Give the position of every Plasmodium parasite visible.
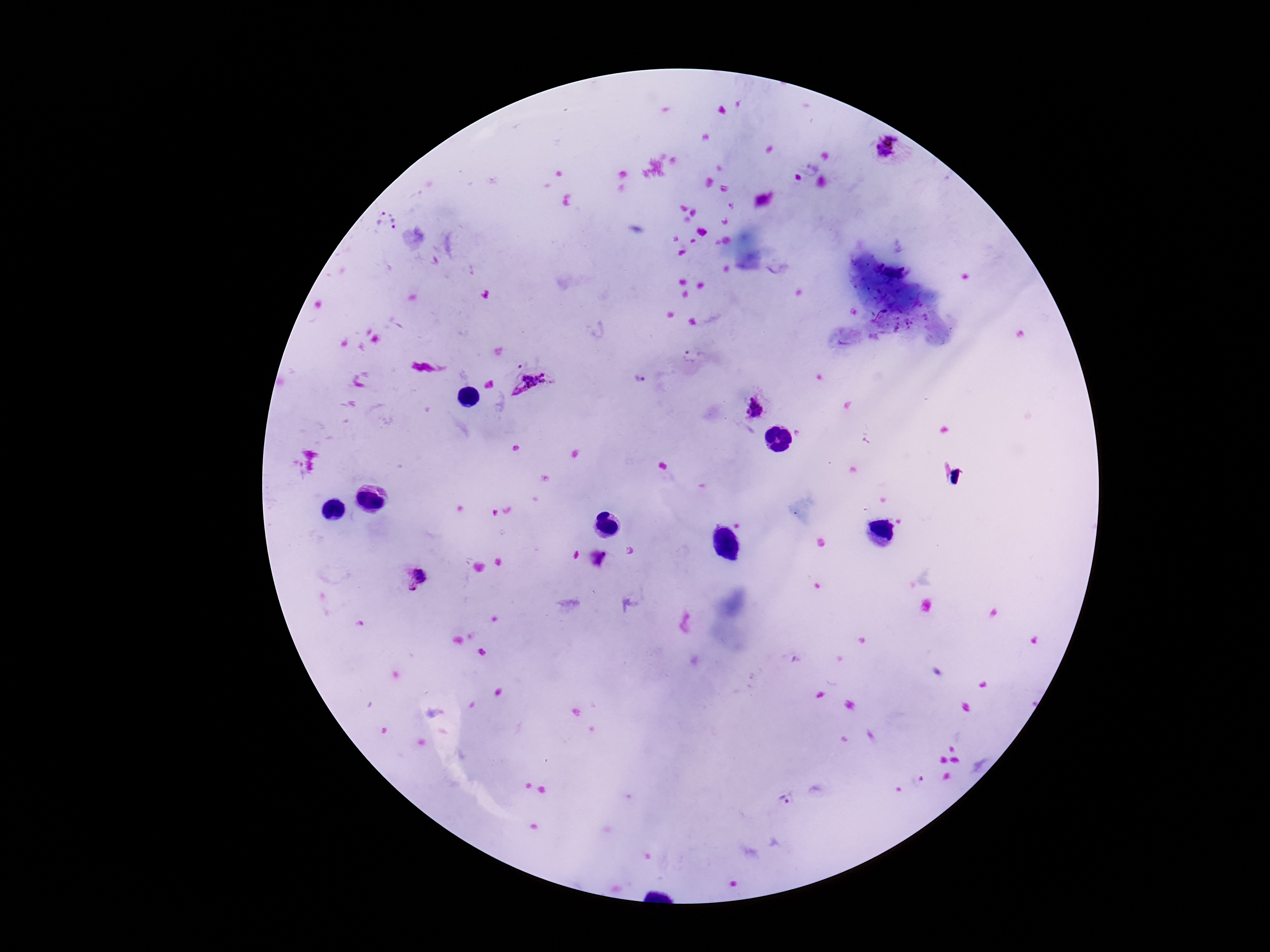

Approximate centers as {x, y} in pixels.
Plasmodium parasites: {885, 147}, {380, 215}, {398, 223}, {687, 357}, {639, 379}, {532, 385}, {755, 411}, {599, 558}, {415, 580}, {916, 781}, {786, 803}.

Summary:
  - Field of view: single
  - Patient malaria status: infected
  - Magnification: 100x
  - Image size: 1270×952 pixels
  - Capture: smartphone camera through the microscope eyepiece
  - Stain: Giemsa
  - Preparation: thick blood film